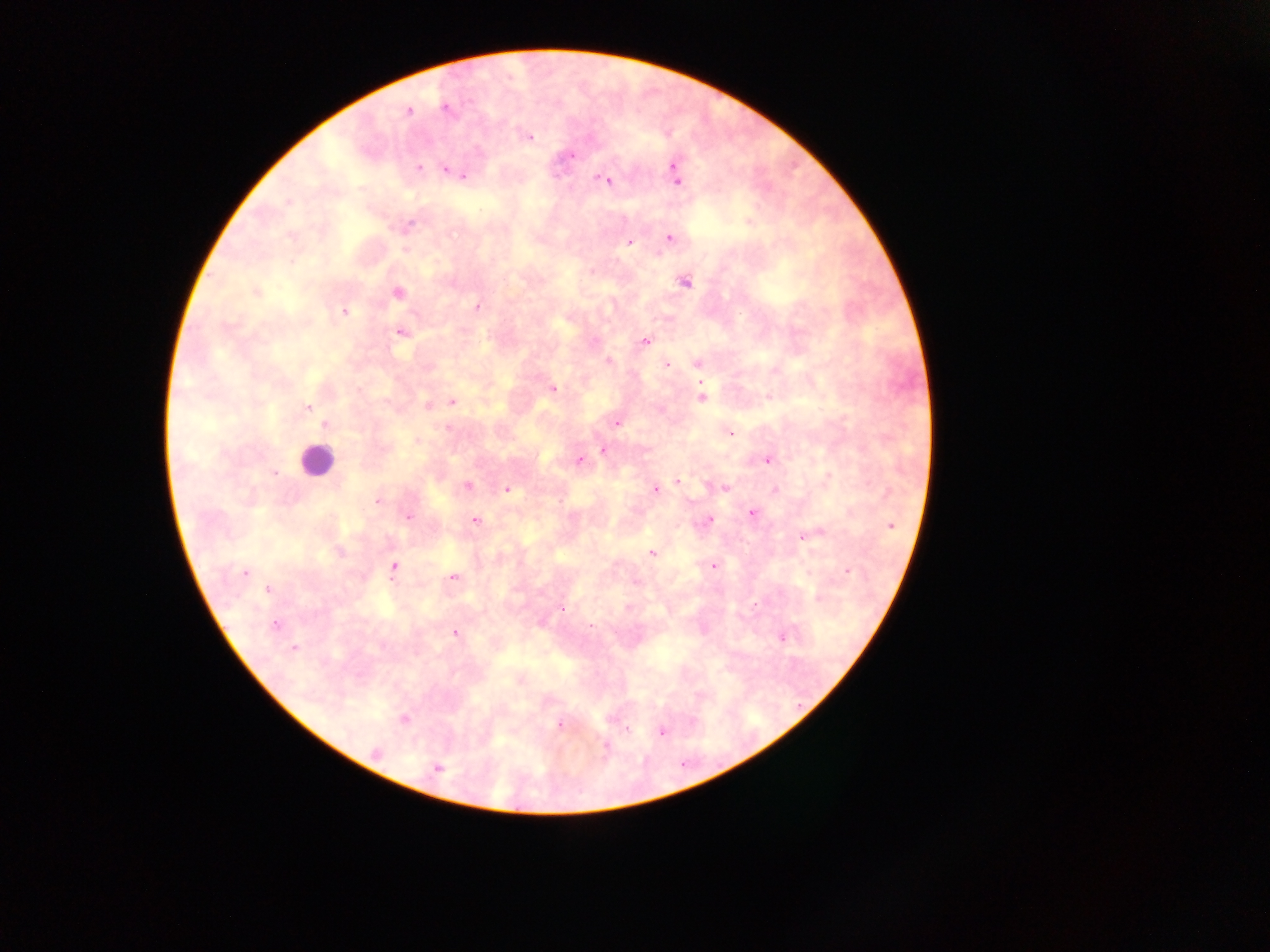
Approximate centers as (x, y) in pixels.
Summary:
  - Plasmodium parasite locations: (446, 109), (409, 111), (529, 137), (571, 155), (419, 167), (446, 170), (456, 173), (675, 173), (463, 175), (599, 179), (605, 180), (677, 181), (287, 202), (409, 225), (670, 238), (630, 243), (685, 282), (256, 292), (397, 292), (477, 306), (344, 311), (401, 332), (646, 341), (609, 361), (698, 363), (666, 365), (553, 389), (701, 397), (451, 402), (428, 405), (307, 407), (617, 423), (325, 425), (447, 429), (731, 433), (603, 450), (579, 460), (767, 460), (275, 473), (677, 482), (467, 486), (724, 488), (507, 490), (655, 490), (775, 490), (377, 500), (752, 513), (408, 517), (475, 521), (708, 521), (891, 526), (820, 532), (803, 536), (339, 551), (651, 553), (713, 565), (394, 567), (848, 572), (245, 573), (451, 577), (269, 589), (819, 597), (561, 610), (275, 625), (455, 634), (782, 638), (294, 649), (404, 719), (559, 723), (627, 729), (662, 732), (606, 746), (376, 753), (437, 768)
  - Leukocyte locations: (316, 460)
  - Country: Ghana
  - Image size: 1270×952 pixels
  - Capture: mobile-phone photograph through a microscope
  - Field of view: single
  - Preparation: thick blood film